Mark where platelets are.
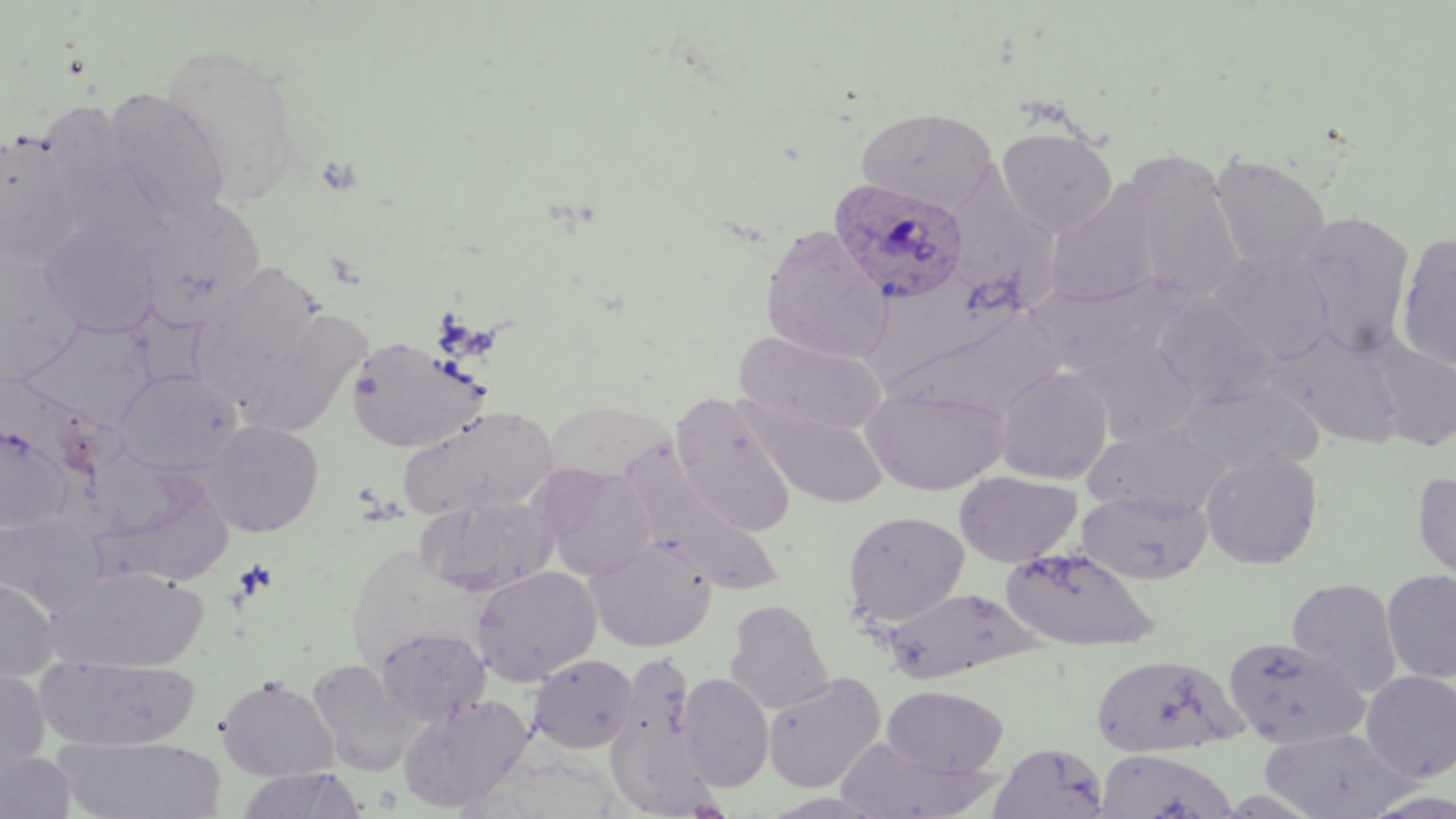

Approximate bounding boxes as named x1/y1/x2/y2 corners in pixels.
Platelets: (x1=317, y1=153, x2=360, y2=195), (x1=233, y1=559, x2=278, y2=603).

Summary:
  - Uninfected red blood cell locations: (x1=160, y1=42, x2=304, y2=206), (x1=103, y1=88, x2=231, y2=222), (x1=856, y1=107, x2=997, y2=212), (x1=40, y1=110, x2=168, y2=248), (x1=997, y1=126, x2=1117, y2=238), (x1=0, y1=129, x2=84, y2=267), (x1=1124, y1=151, x2=1245, y2=304), (x1=1208, y1=152, x2=1331, y2=272), (x1=945, y1=163, x2=1066, y2=310), (x1=1045, y1=182, x2=1161, y2=307), (x1=136, y1=196, x2=266, y2=329), (x1=1294, y1=211, x2=1416, y2=354), (x1=40, y1=222, x2=159, y2=338), (x1=760, y1=226, x2=892, y2=363), (x1=1395, y1=232, x2=1455, y2=371), (x1=1209, y1=248, x2=1335, y2=362), (x1=0, y1=256, x2=85, y2=383), (x1=193, y1=261, x2=322, y2=391), (x1=870, y1=270, x2=1004, y2=384), (x1=1028, y1=275, x2=1182, y2=376), (x1=1151, y1=292, x2=1277, y2=407), (x1=233, y1=308, x2=369, y2=440), (x1=897, y1=308, x2=1067, y2=420), (x1=22, y1=322, x2=156, y2=430), (x1=1264, y1=326, x2=1403, y2=447), (x1=735, y1=331, x2=887, y2=437), (x1=345, y1=336, x2=486, y2=452), (x1=1367, y1=338, x2=1456, y2=451), (x1=1069, y1=340, x2=1201, y2=446), (x1=994, y1=367, x2=1113, y2=484), (x1=116, y1=368, x2=242, y2=476), (x1=1178, y1=381, x2=1323, y2=475), (x1=862, y1=384, x2=1009, y2=495), (x1=670, y1=394, x2=798, y2=536), (x1=749, y1=401, x2=889, y2=509), (x1=542, y1=402, x2=672, y2=482), (x1=399, y1=406, x2=558, y2=520), (x1=201, y1=419, x2=324, y2=537), (x1=0, y1=422, x2=72, y2=533), (x1=1084, y1=423, x2=1230, y2=519), (x1=1201, y1=450, x2=1323, y2=569), (x1=534, y1=463, x2=657, y2=581), (x1=630, y1=463, x2=784, y2=597), (x1=954, y1=471, x2=1081, y2=568), (x1=1412, y1=472, x2=1456, y2=597), (x1=100, y1=473, x2=237, y2=584), (x1=1077, y1=488, x2=1212, y2=585), (x1=419, y1=494, x2=558, y2=597), (x1=843, y1=511, x2=969, y2=627), (x1=0, y1=512, x2=105, y2=614), (x1=585, y1=536, x2=717, y2=653), (x1=1001, y1=545, x2=1158, y2=652), (x1=470, y1=565, x2=602, y2=687), (x1=48, y1=567, x2=207, y2=673), (x1=1382, y1=568, x2=1456, y2=683), (x1=1287, y1=577, x2=1403, y2=696), (x1=0, y1=578, x2=59, y2=682), (x1=880, y1=586, x2=1038, y2=682), (x1=725, y1=599, x2=833, y2=714), (x1=374, y1=627, x2=490, y2=726), (x1=1222, y1=636, x2=1370, y2=748), (x1=1091, y1=653, x2=1243, y2=758), (x1=35, y1=654, x2=201, y2=752), (x1=529, y1=654, x2=638, y2=754), (x1=307, y1=659, x2=416, y2=776), (x1=0, y1=667, x2=50, y2=781), (x1=1360, y1=669, x2=1456, y2=782), (x1=677, y1=672, x2=774, y2=790), (x1=762, y1=672, x2=886, y2=794), (x1=216, y1=674, x2=338, y2=782), (x1=881, y1=684, x2=1008, y2=776), (x1=397, y1=694, x2=533, y2=813), (x1=1259, y1=727, x2=1413, y2=818), (x1=55, y1=735, x2=225, y2=818), (x1=833, y1=737, x2=997, y2=818), (x1=989, y1=741, x2=1110, y2=818), (x1=1094, y1=748, x2=1239, y2=819), (x1=0, y1=750, x2=76, y2=819), (x1=235, y1=767, x2=365, y2=819)
  - Plasmodium ovale-infected red blood cell locations: (x1=829, y1=177, x2=969, y2=304)
  - Slide-level diagnosis: Plasmodium ovale
  - Magnification: 1000x
  - Field of view: single
  - Stain: May-Grünwald-Giemsa
  - Modality: optical microscopy
  - Preparation: thin blood film
  - Image size: 1456×819 pixels